Name the cell type shown.
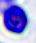
This is a leukocyte.

Summary:
  - Modality: micrograph
  - Magnification: 400x